Name the parasite shown.
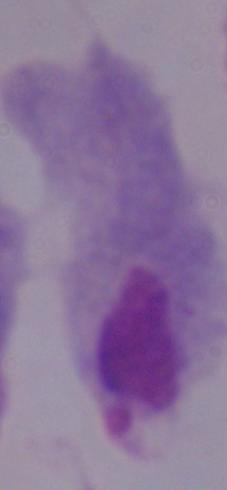
This is a trichomonad.

Summary:
  - Modality: micrograph
  - Magnification: 1000x